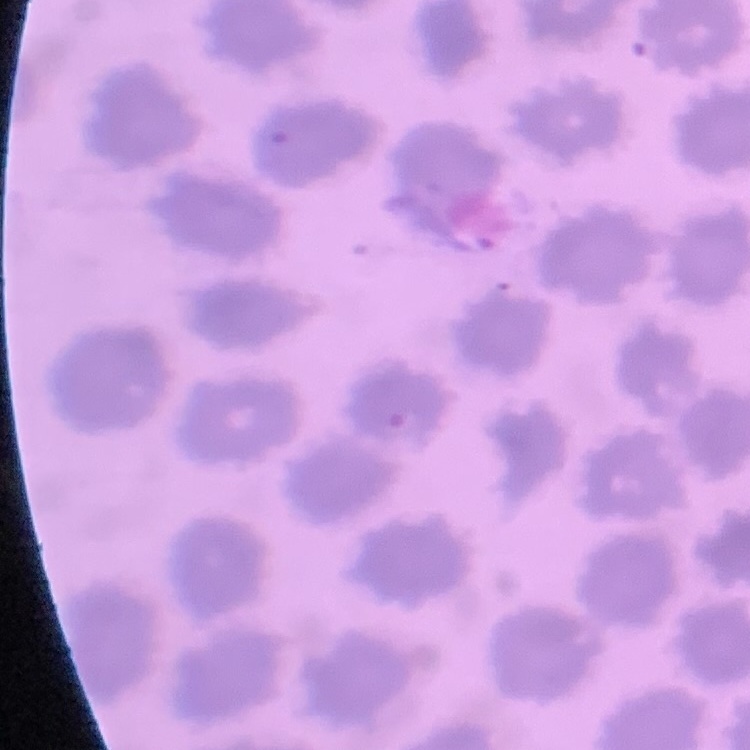

erythrocyte morphology = no rouleaux formation
stain = Field's or Giemsa
image type = square crop of a larger photomicrograph
preparation = thin peripheral smear